Locate every malaria parasite.
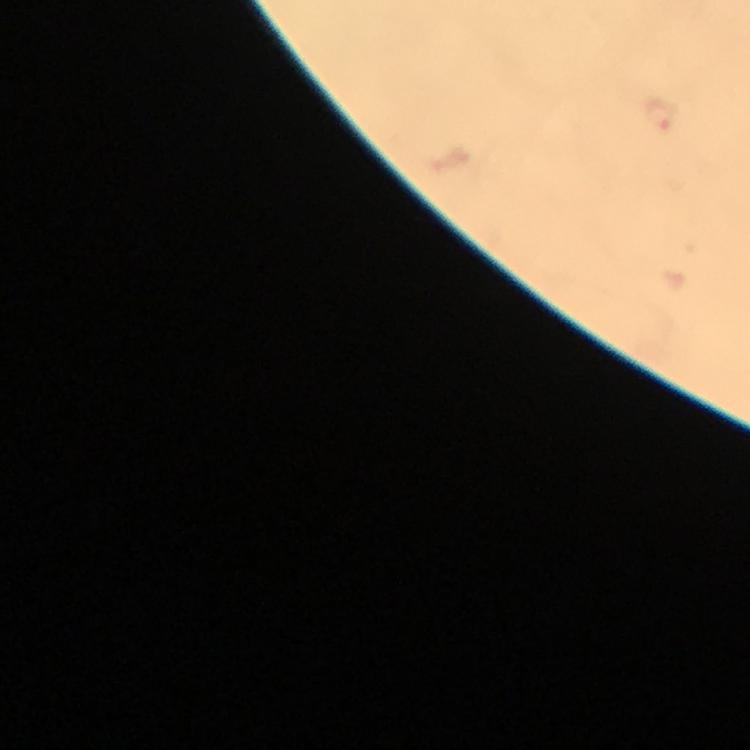
Approximate object centers, in pixels from the top-left corner.
Malaria parasites: (x=661, y=115).

stain = Giemsa
image size = 750×750 pixels
immersion oil = applied
capture = smartphone mounted on the microscope
magnification = 100x
preparation = thick smear
cropped from = one field of view
context = from a diagnostic examination for malaria